Name the parasite shown.
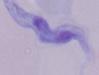

This is a trypanosome.

magnification = 1000x
modality = micrograph